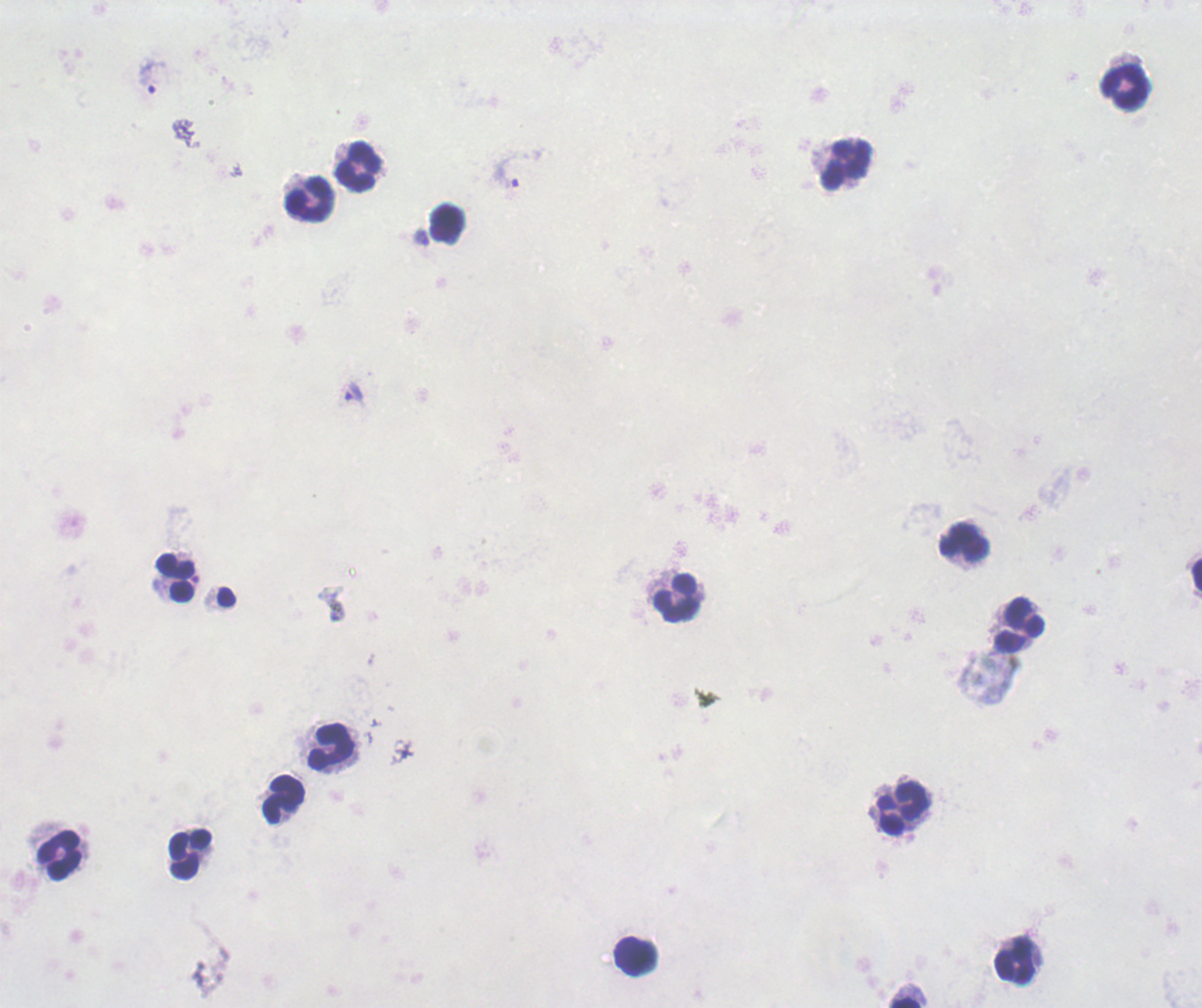
Approximate object centers, in pixels from the top-left corner.
Summary:
  - Leukocyte locations: (x=1125, y=87), (x=847, y=164), (x=357, y=166), (x=310, y=199), (x=447, y=224), (x=963, y=542), (x=1197, y=573), (x=174, y=578), (x=676, y=599), (x=1018, y=625), (x=330, y=745), (x=284, y=799), (x=902, y=809), (x=190, y=853), (x=59, y=855), (x=635, y=956), (x=1015, y=961), (x=904, y=1001)
  - Trophozoite locations: (x=152, y=77), (x=506, y=172), (x=355, y=391)
  - Stain: Romanowsky
  - Context: previously used in a real diagnosis
  - Background quality: poor
  - Field of view: one from this slide
  - Magnification: 100x
  - Result: positive for malaria parasites
  - Preparation: thick blood smear
  - Image size: 1202×1008 pixels